Give the extent of all uninfected red blood cells.
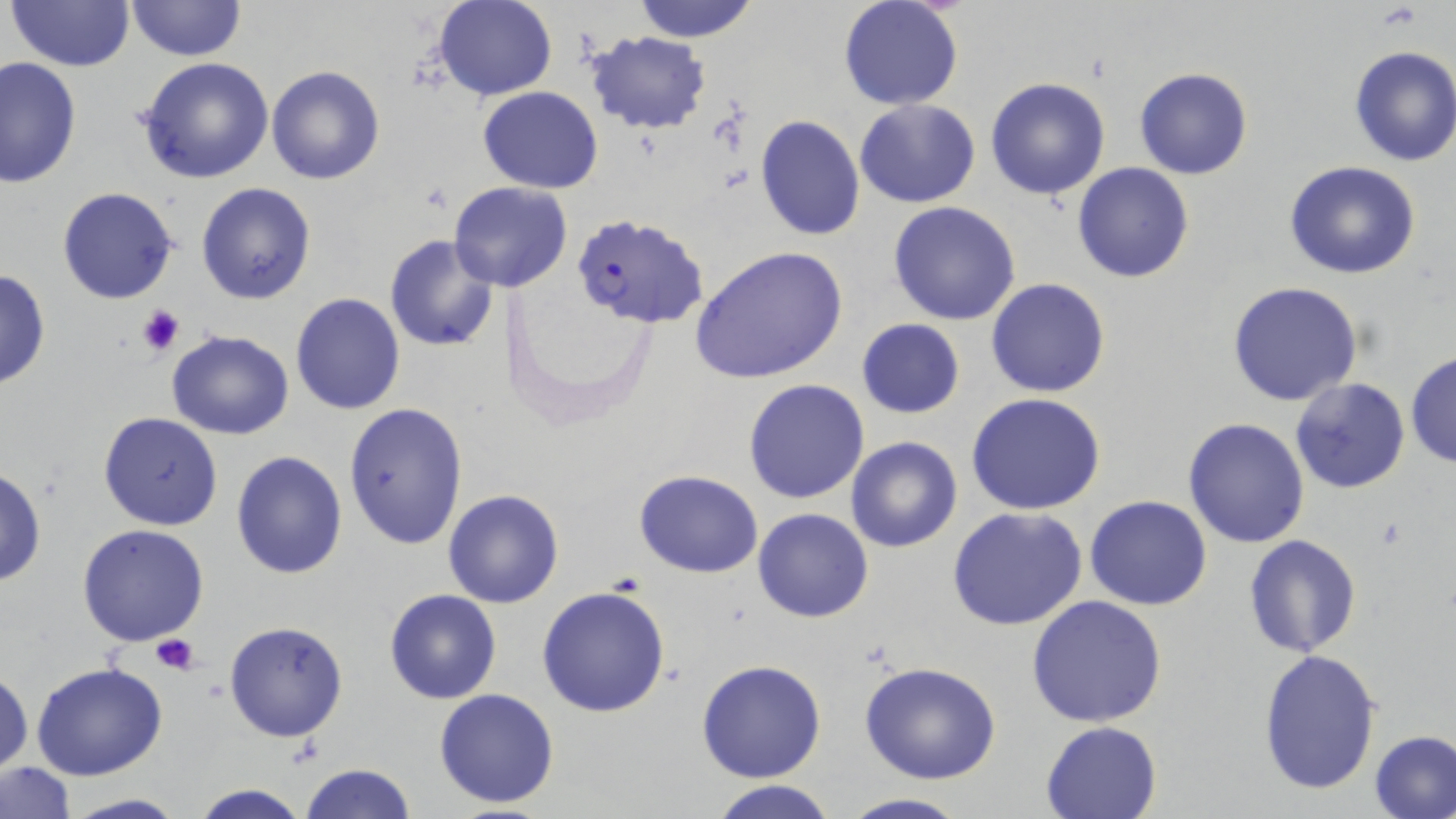

Approximate bounding boxes as [x1, y1, x2, y2] in pixels.
Uninfected red blood cells: [5, 0, 134, 71], [630, 0, 761, 42], [124, 1, 247, 61], [432, 1, 557, 100], [837, 1, 964, 111], [585, 31, 711, 133], [1348, 45, 1456, 167], [0, 56, 80, 189], [135, 56, 275, 183], [266, 64, 385, 185], [1135, 68, 1253, 180], [986, 77, 1111, 200], [478, 87, 604, 193], [855, 99, 982, 207], [754, 116, 864, 241], [1072, 162, 1195, 282], [1283, 162, 1423, 280], [195, 182, 316, 304], [448, 182, 574, 293], [57, 187, 179, 304], [888, 201, 1022, 325], [383, 234, 500, 353], [690, 246, 849, 384], [0, 268, 51, 391], [986, 278, 1110, 398], [1227, 281, 1364, 406], [289, 292, 406, 416], [856, 319, 965, 418], [165, 330, 294, 440], [1405, 351, 1456, 470], [744, 379, 870, 503], [1290, 379, 1410, 495], [965, 392, 1106, 516], [344, 401, 469, 550], [98, 412, 223, 531], [1182, 418, 1310, 548], [845, 436, 963, 553], [230, 450, 347, 579], [0, 466, 46, 587], [633, 469, 764, 578], [442, 489, 564, 608], [1084, 494, 1213, 610], [752, 507, 873, 623], [947, 507, 1090, 631], [76, 524, 209, 646], [1244, 535, 1363, 659], [537, 585, 672, 719], [384, 589, 501, 704], [1025, 593, 1168, 727], [225, 619, 349, 741], [1257, 648, 1382, 797], [696, 659, 827, 781], [29, 662, 169, 782], [858, 662, 1003, 786], [0, 667, 33, 778], [433, 687, 561, 809], [1040, 719, 1165, 818], [1370, 731, 1456, 818], [2, 761, 76, 817], [300, 763, 417, 818], [705, 778, 844, 819], [189, 783, 311, 819], [56, 792, 190, 819], [835, 793, 973, 819].

Plasmodium falciparum-infected red blood cell locations: [577, 218, 712, 334]. Platelet locations: [134, 303, 186, 358], [150, 635, 200, 675]. Slide-level diagnosis: Plasmodium falciparum. Image is 1456×819 pixels. May-Grünwald-Giemsa stain. Thin blood film. 1000x magnification. One field of a larger specimen. Optical microscopy.